Classify this cell by malaria status.
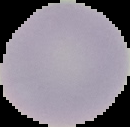

It is uninfected.

preparation: thin blood film
image_size: 130×127 pixels
image_type: segmented cell region with the area outside set to black